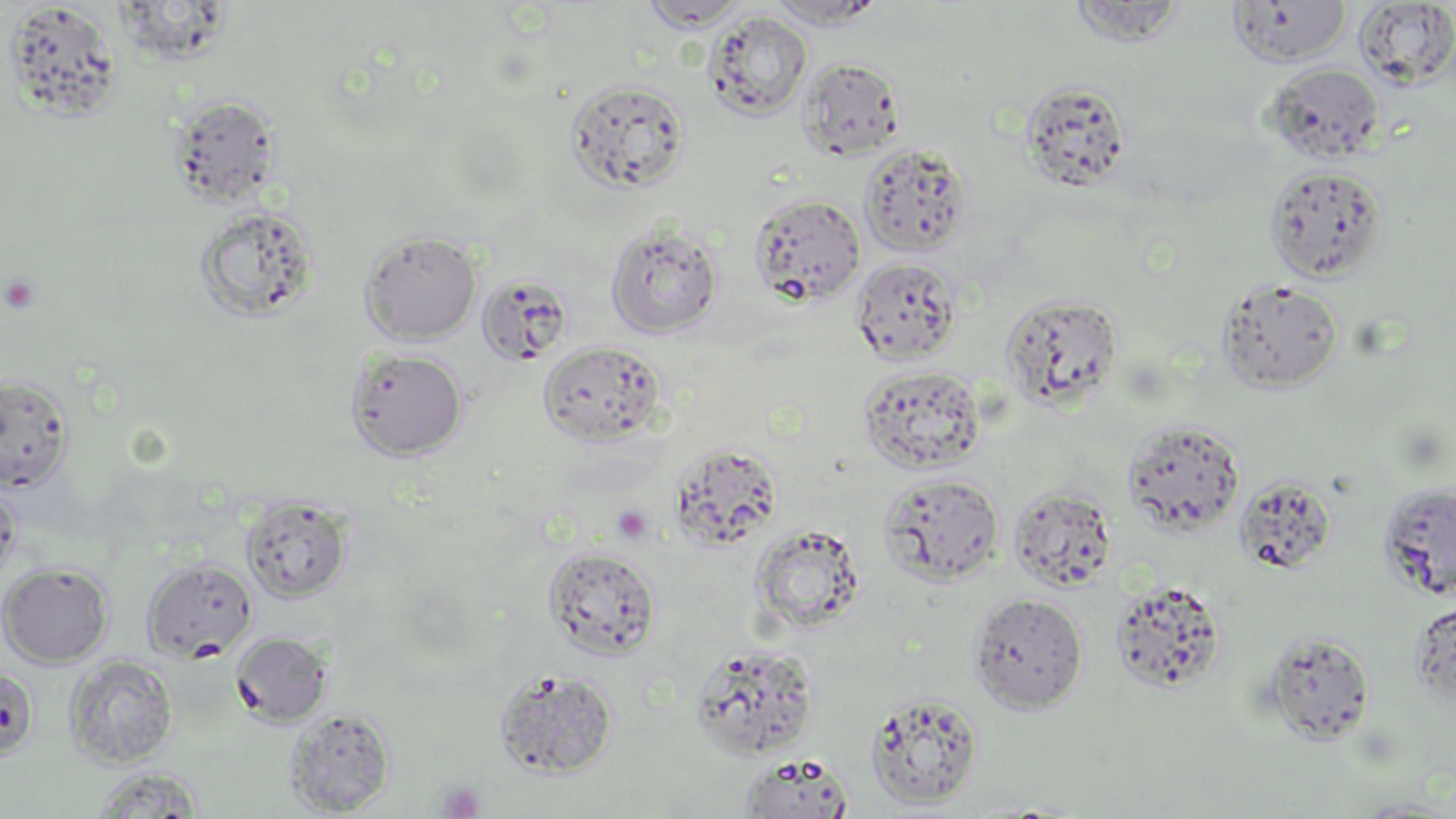
slide_level_diagnosis: negative for blood parasites
modality: light microscopy
field_of_view: single
stain: May-Grünwald-Giemsa
uninfected_red_blood_cell_locations: 'approximate bounding boxes as (x1,y1)-(x2,y2) corner pairs in pixels: (767,0)-(888,28), (639,1)-(749,31), (1066,1)-(1189,47), (1226,1)-(1352,67), (1354,1)-(1456,89), (4,2)-(124,121), (704,10)-(813,121), (798,57)-(906,161), (1265,62)-(1385,164), (565,78)-(691,193), (1020,80)-(1132,193), (168,94)-(282,209), (859,142)-(972,257), (1264,165)-(1387,282), (748,193)-(866,307), (195,206)-(319,323), (605,219)-(723,338), (360,229)-(482,344), (850,256)-(962,366), (476,275)-(574,366), (1217,279)-(1344,392), (999,292)-(1124,412), (538,340)-(667,446), (345,348)-(467,460), (858,365)-(986,474), (0,374)-(74,492), (1121,418)-(1245,536), (669,441)-(783,550), (878,472)-(1004,586), (1234,475)-(1337,575), (1378,482)-(1456,598), (0,484)-(21,587), (1008,484)-(1117,592), (241,495)-(353,604), (750,523)-(866,635), (543,547)-(663,659), (141,558)-(258,662), (0,562)-(114,667), (1109,578)-(1228,694), (968,592)-(1088,714), (1408,597)-(1456,710), (1261,630)-(1376,745), (230,631)-(333,727), (688,642)-(821,761), (64,655)-(178,768), (0,667)-(38,760), (494,667)-(618,779), (864,691)-(985,809), (284,709)-(395,816), (738,753)-(855,818), (92,767)-(205,816), (1347,798)-(1456,817)'
magnification: 1000x
platelet_locations: 'approximate bounding boxes as (x1,y1)-(x2,y2) corner pairs in pixels: (1,274)-(42,314), (612,505)-(653,544), (436,781)-(485,819)'
preparation: thin blood film
image_size: 1456×819 pixels